Report the malaria status of this cell.
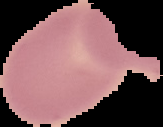

Uninfected.

Image is 163×127 pixels. The area outside the segmented cell region is set to black. From a thin blood smear.